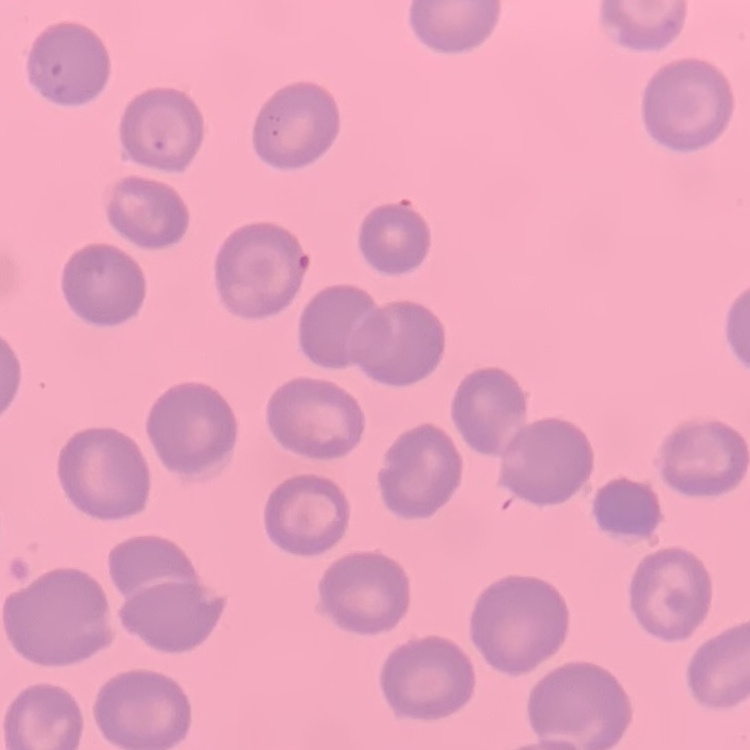

Summary:
  - Red blood cell morphology: no rouleaux formation
  - Image type: square crop of a larger photomicrograph
  - Stain: Field's or Giemsa
  - Preparation: thin blood film